Classify this cell by malaria status.
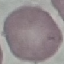

It is uninfected.

Acquired by smartphone through the microscope eyepiece. Giemsa stain. Cell patch, automatically extracted from a larger field of view and resized to 64 × 64 pixels. Thin smear of blood.